Outline each Plasmodium falciparum-infected red blood cell.
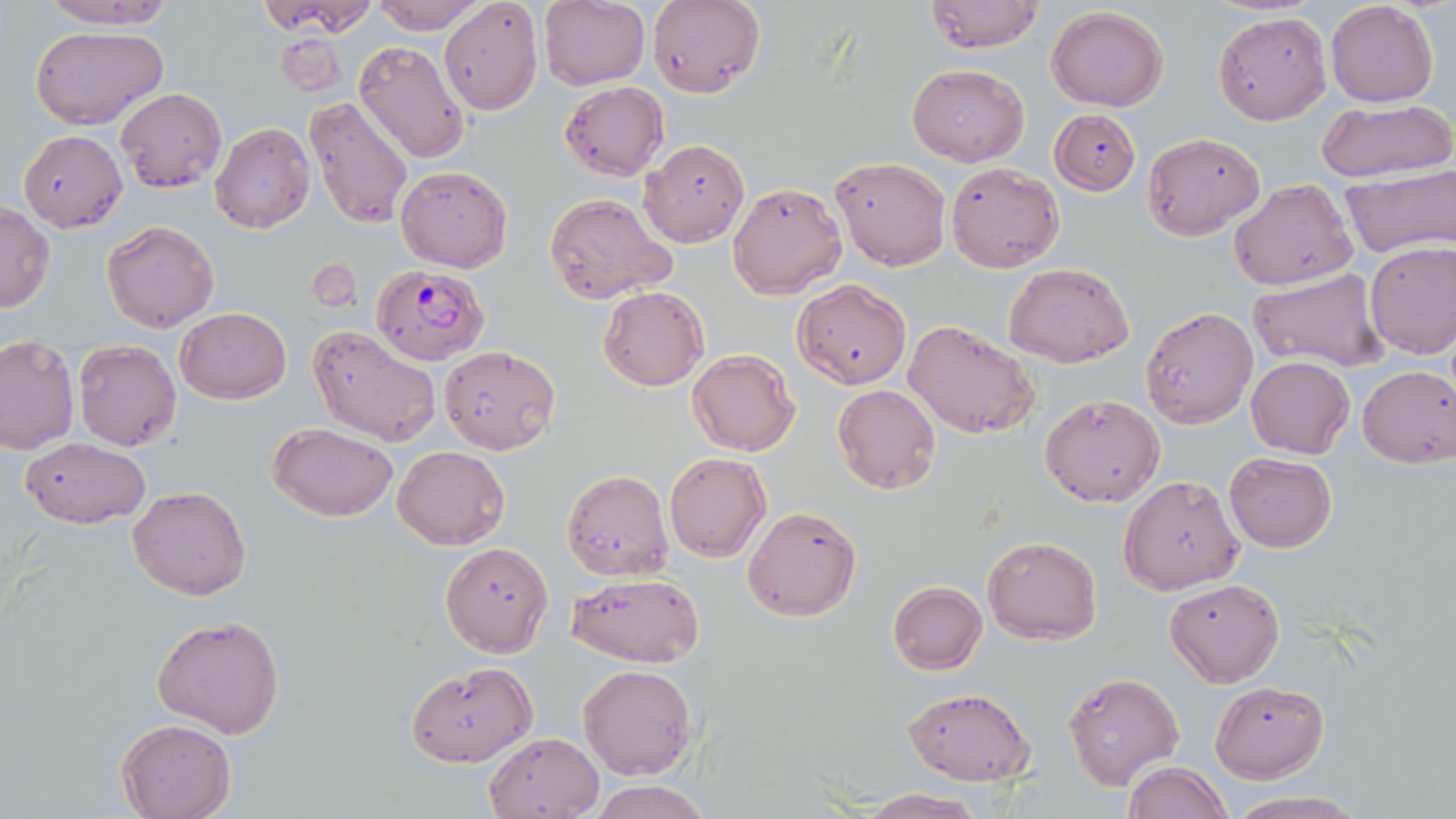
Approximate bounding boxes as (x1, y1, x2, y2) in pixels.
Plasmodium falciparum-infected red blood cells: (372, 265, 489, 365).

Uninfected red blood cell locations: (32, 0, 176, 28), (255, 0, 378, 38), (371, 0, 481, 31), (438, 0, 543, 115), (538, 0, 651, 91), (648, 0, 765, 98), (923, 1, 1045, 53), (1325, 1, 1440, 107), (1046, 6, 1170, 112), (1212, 11, 1331, 126), (31, 25, 167, 129), (275, 33, 347, 96), (353, 41, 471, 167), (907, 63, 1029, 166), (560, 81, 668, 180), (115, 88, 227, 193), (304, 97, 413, 229), (1315, 97, 1454, 183), (1050, 108, 1141, 196), (210, 123, 315, 233), (1142, 129, 1265, 239), (19, 130, 127, 232), (638, 139, 748, 246), (830, 156, 949, 271), (947, 161, 1064, 274), (394, 164, 513, 272), (1339, 164, 1454, 259), (1230, 178, 1358, 290), (728, 180, 847, 300), (542, 192, 675, 303), (0, 200, 54, 313), (102, 219, 218, 332), (1364, 241, 1456, 358), (1003, 262, 1135, 367), (1249, 268, 1390, 373), (793, 279, 911, 388), (597, 286, 709, 392), (176, 306, 291, 404), (1139, 306, 1257, 430), (904, 318, 1039, 439), (306, 325, 441, 446), (0, 334, 79, 454), (72, 339, 181, 451), (438, 345, 559, 455), (686, 349, 800, 456), (1246, 356, 1354, 459), (1358, 364, 1456, 468), (832, 383, 941, 494), (1038, 393, 1164, 507), (267, 421, 398, 522), (20, 436, 150, 528), (392, 445, 509, 549), (664, 451, 771, 562), (1224, 451, 1335, 553), (560, 469, 673, 583), (1119, 473, 1245, 595), (128, 485, 250, 600), (742, 504, 861, 622), (983, 535, 1101, 644), (441, 542, 553, 656), (569, 573, 705, 667), (1165, 578, 1285, 686), (887, 581, 987, 674), (152, 614, 285, 738), (404, 662, 537, 767), (578, 664, 697, 780), (1061, 672, 1184, 792), (1210, 682, 1327, 782), (901, 687, 1037, 786), (116, 718, 237, 819), (483, 732, 603, 818), (1123, 760, 1232, 819), (588, 780, 710, 819), (855, 789, 987, 818), (1221, 792, 1372, 819). Slide-level diagnosis: Plasmodium falciparum. One field of a larger specimen. Captured at 1000x magnification. Light microscopy. Thin blood smear. Image is 1456×819 pixels. May-Grünwald-Giemsa-stained preparation.